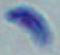

{
  "magnification": "1000x",
  "modality": "micrograph",
  "identification": "Toxoplasma gondii"
}